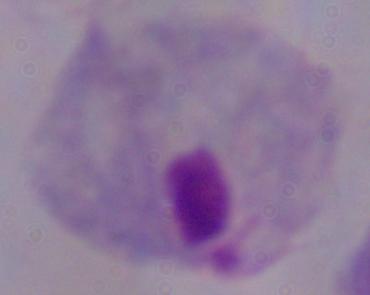

{
  "modality": "micrograph",
  "identification": "trichomonad",
  "magnification": "1000x"
}